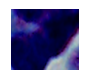

A leukocyte is shown. 1000x magnification. Photomicrograph.